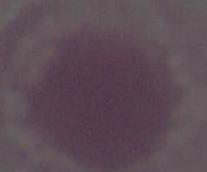
{
  "magnification": "1000x",
  "identification": "red blood cell",
  "modality": "photomicrograph"
}